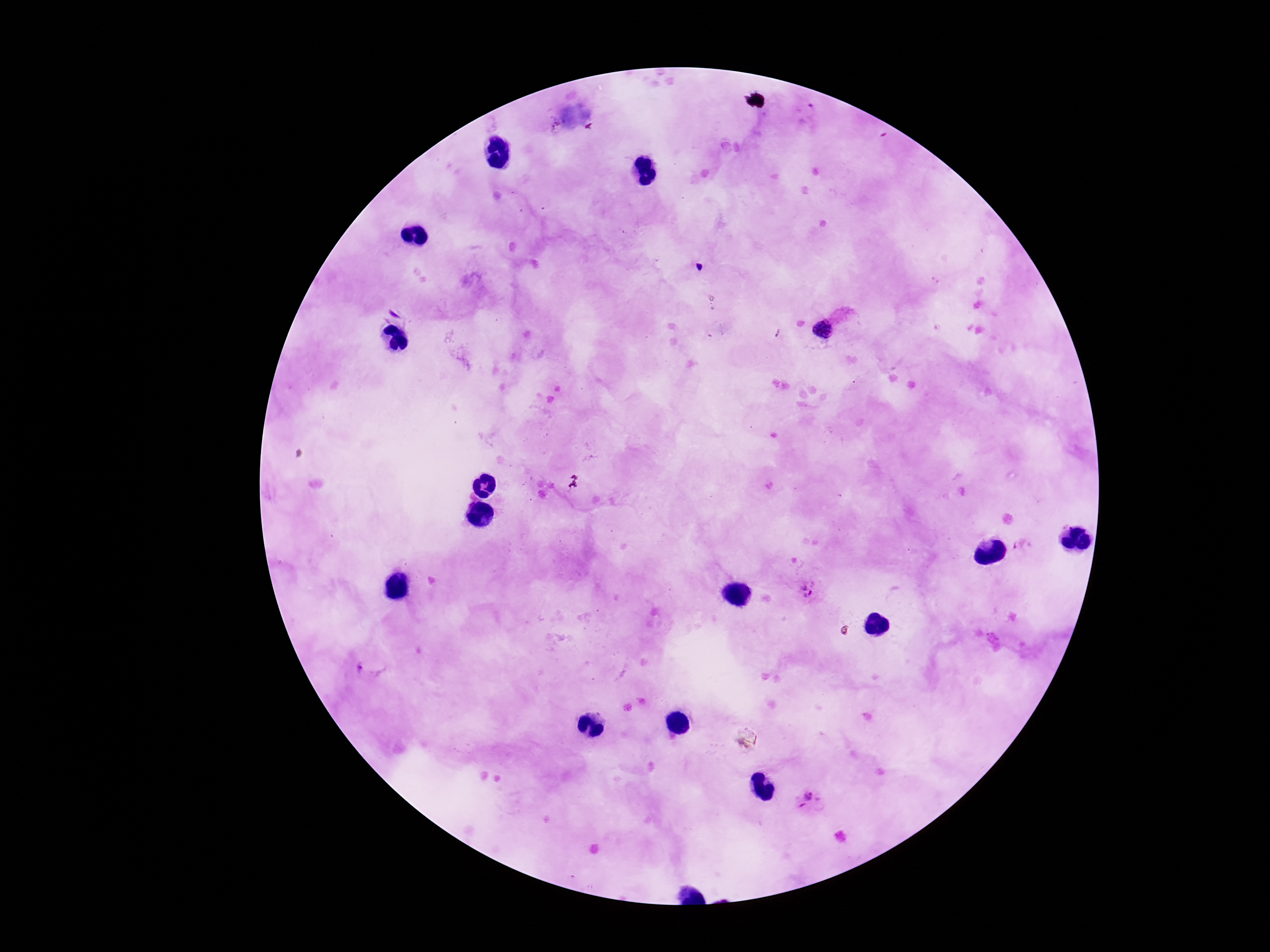
{
  "patient_malaria_status": "infected",
  "stain": "Giemsa",
  "field_of_view": "one from this slide",
  "preparation": "thick peripheral-blood smear",
  "capture": "smartphone camera through the microscope eyepiece",
  "image_size": "1270×952 pixels",
  "plasmodium_parasite_locations": "approximate object centers, in pixels from the top-left corner: (x=821, y=327), (x=1022, y=545), (x=809, y=587), (x=369, y=666), (x=811, y=802)",
  "magnification": "100x"
}